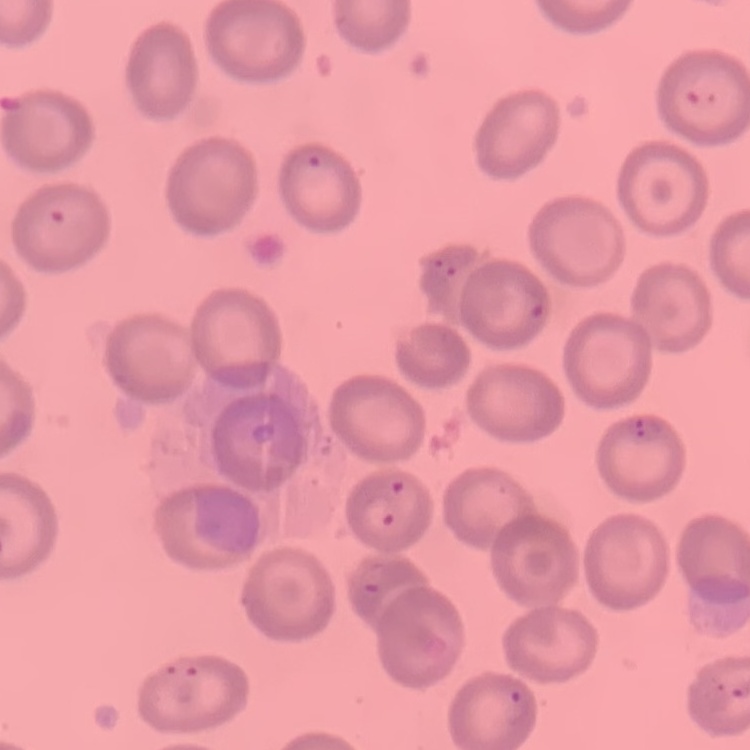

red blood cell morphology = no rouleaux formation
image type = one tile cut from a larger photomicrograph
preparation = thin blood smear
stain = Field's or Giemsa